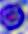
Summary:
  - Modality: micrograph
  - Identification: leukocyte
  - Magnification: 400x